Report the malaria status of this cell.
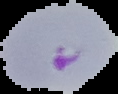
It is parasitized.

Segmented cell region on a black background. Image is 118×94 pixels. From a thin blood film.